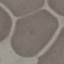

Result: no malaria parasites seen. Thin smear of blood. Acquired by smartphone through the microscope eyepiece. Giemsa-stained preparation. Cell patch, automatically extracted from a larger field of view and resized to 64 × 64 pixels.